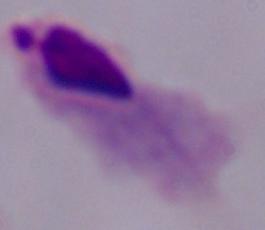
modality = photomicrograph
magnification = 1000x
identification = trichomonad